Give the extent of all Plasmodium ovale-infected red blood cells.
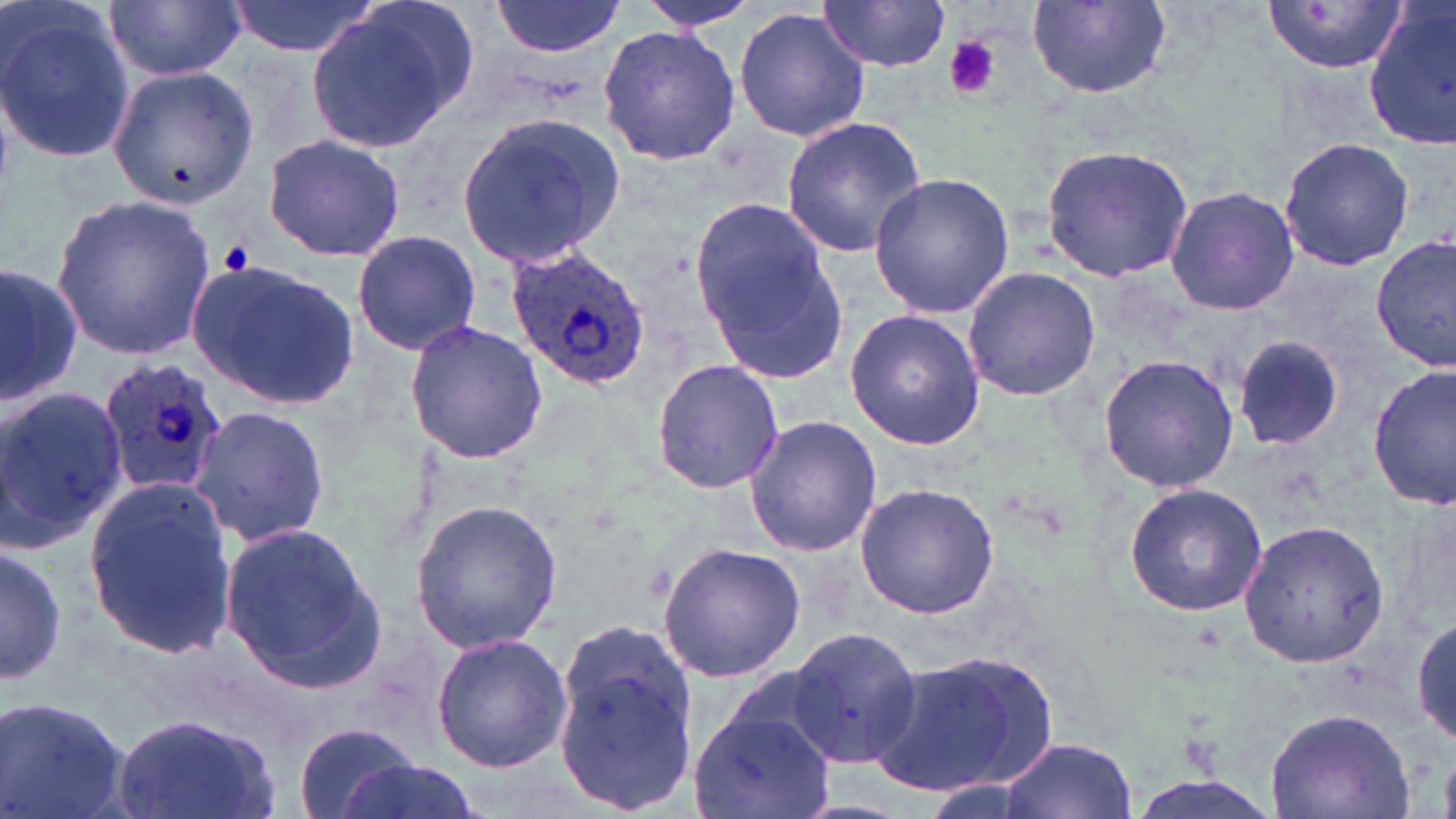
Approximate bounding boxes as named x1/y1/x2/y2 corners in pixels.
Plasmodium ovale-infected red blood cells: (x1=504, y1=244, x2=651, y2=388), (x1=97, y1=355, x2=227, y2=498).

slide-level diagnosis = Plasmodium ovale
platelet locations = approximate bounding boxes as named x1/y1/x2/y2 corners in pixels: (x1=942, y1=35, x2=1001, y2=99), (x1=222, y1=241, x2=257, y2=274)
field of view = single
magnification = 1000x
stain = May-Grünwald-Giemsa
image size = 1456×819 pixels
preparation = thin blood film
modality = light microscopy
uninfected red blood cell locations = approximate bounding boxes as named x1/y1/x2/y2 corners in pixels: (x1=0, y1=0, x2=136, y2=167), (x1=106, y1=0, x2=244, y2=82), (x1=224, y1=0, x2=379, y2=57), (x1=640, y1=0, x2=757, y2=30), (x1=490, y1=1, x2=626, y2=56), (x1=818, y1=1, x2=954, y2=70), (x1=1263, y1=1, x2=1407, y2=77), (x1=1363, y1=1, x2=1456, y2=148), (x1=304, y1=2, x2=476, y2=152), (x1=1029, y1=2, x2=1172, y2=100), (x1=734, y1=7, x2=871, y2=143), (x1=596, y1=23, x2=739, y2=167), (x1=104, y1=59, x2=260, y2=212), (x1=455, y1=110, x2=626, y2=271), (x1=779, y1=117, x2=928, y2=257), (x1=261, y1=134, x2=405, y2=263), (x1=1279, y1=136, x2=1414, y2=271), (x1=1040, y1=145, x2=1195, y2=284), (x1=868, y1=171, x2=1015, y2=320), (x1=1165, y1=186, x2=1299, y2=315), (x1=50, y1=196, x2=217, y2=358), (x1=689, y1=199, x2=848, y2=383), (x1=351, y1=230, x2=482, y2=356), (x1=1372, y1=234, x2=1454, y2=373), (x1=185, y1=259, x2=359, y2=410), (x1=0, y1=263, x2=80, y2=408), (x1=960, y1=266, x2=1102, y2=401), (x1=845, y1=310, x2=986, y2=450), (x1=404, y1=319, x2=549, y2=466), (x1=1231, y1=337, x2=1346, y2=451), (x1=1098, y1=353, x2=1240, y2=493), (x1=650, y1=360, x2=784, y2=495), (x1=1368, y1=364, x2=1456, y2=511), (x1=0, y1=385, x2=126, y2=550), (x1=185, y1=403, x2=332, y2=548), (x1=743, y1=415, x2=882, y2=557), (x1=80, y1=475, x2=235, y2=660), (x1=1121, y1=481, x2=1268, y2=617), (x1=853, y1=482, x2=1000, y2=618), (x1=410, y1=498, x2=561, y2=655), (x1=217, y1=519, x2=388, y2=694), (x1=1238, y1=519, x2=1390, y2=670), (x1=1, y1=542, x2=65, y2=687), (x1=658, y1=542, x2=806, y2=684), (x1=1412, y1=615, x2=1455, y2=748), (x1=551, y1=620, x2=699, y2=814), (x1=788, y1=626, x2=923, y2=768), (x1=430, y1=632, x2=570, y2=772), (x1=866, y1=648, x2=1062, y2=799), (x1=2, y1=695, x2=132, y2=819), (x1=1265, y1=702, x2=1415, y2=818), (x1=690, y1=705, x2=836, y2=819), (x1=112, y1=710, x2=281, y2=819), (x1=293, y1=723, x2=422, y2=819), (x1=1001, y1=735, x2=1134, y2=816), (x1=329, y1=758, x2=485, y2=819)